Identify the cell.
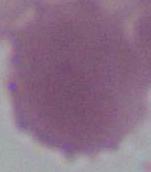

This is an erythrocyte.

{
  "magnification": "1000x",
  "modality": "micrograph"
}